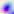

Captured at 400x magnification. Micrograph. Toxoplasma gondii is shown.